Mark where platelets are.
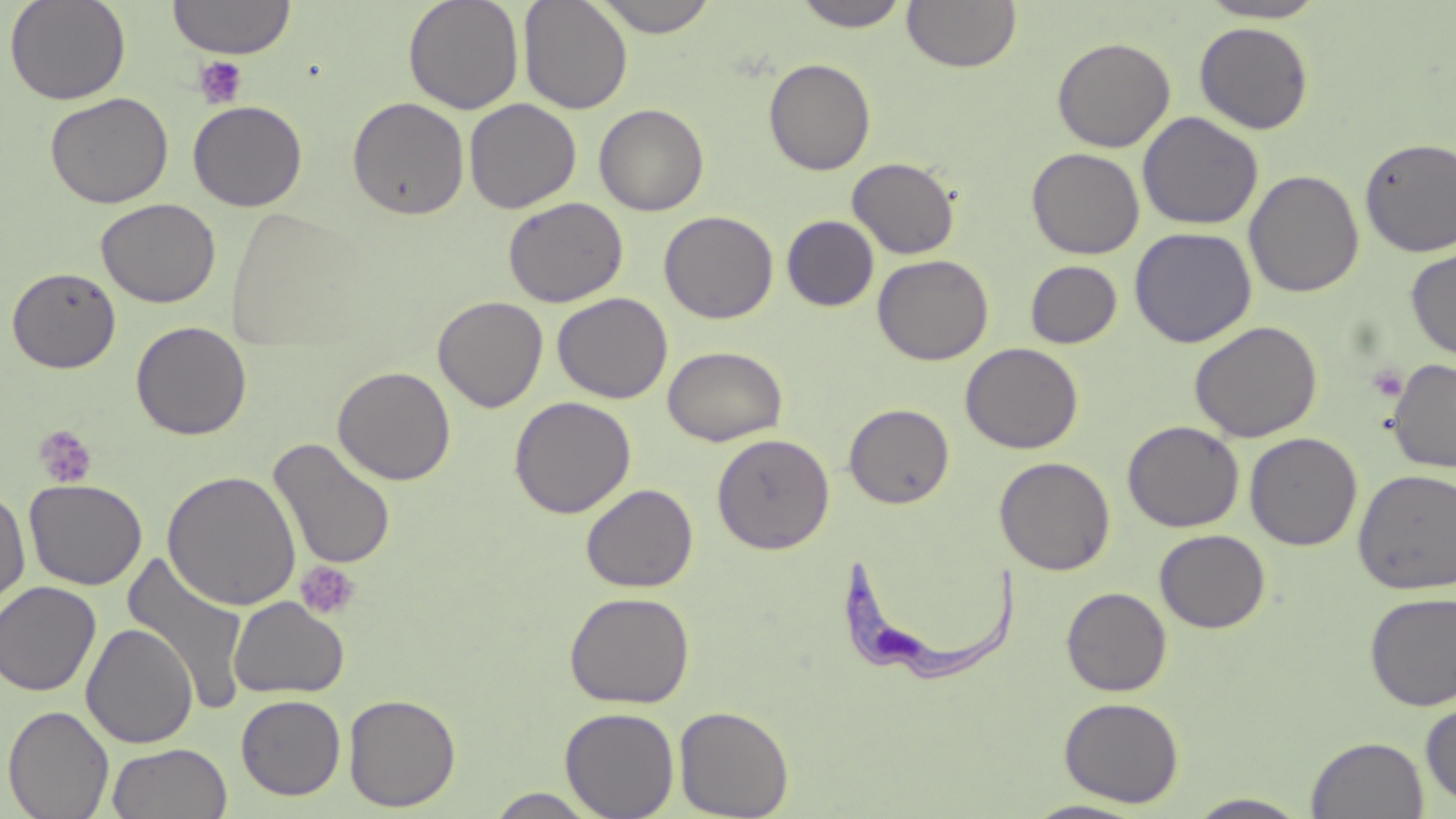

Approximate bounding boxes as (x1, y1, x2, y2) in pixels.
Platelets: (193, 55, 248, 109), (1366, 365, 1409, 402), (34, 425, 97, 489), (295, 561, 361, 621).

Summary:
  - Trypanosoma brucei locations: (844, 553, 1020, 686)
  - Uninfected red blood cell locations: (3, 0, 130, 105), (167, 0, 296, 59), (403, 0, 525, 115), (518, 0, 633, 114), (592, 0, 719, 36), (791, 0, 913, 32), (903, 1, 1021, 73), (1197, 1, 1328, 23), (1194, 21, 1314, 134), (1052, 36, 1175, 152), (764, 58, 876, 175), (45, 92, 174, 209), (347, 96, 470, 220), (464, 98, 582, 214), (188, 100, 307, 211), (594, 103, 709, 216), (1137, 111, 1263, 230), (1358, 136, 1456, 257), (1027, 147, 1145, 259), (848, 157, 960, 259), (1244, 169, 1365, 298), (503, 197, 628, 307), (95, 198, 221, 308), (659, 210, 778, 323), (782, 215, 879, 311), (1130, 227, 1257, 348), (1405, 247, 1456, 362), (873, 254, 994, 365), (1025, 260, 1122, 348), (7, 267, 121, 373), (552, 292, 673, 404), (432, 296, 548, 413), (1189, 320, 1323, 443), (131, 321, 252, 440), (960, 342, 1083, 454), (663, 345, 788, 446), (1387, 358, 1456, 473), (332, 365, 456, 485), (509, 396, 636, 519), (844, 403, 954, 509), (1122, 420, 1244, 532), (711, 432, 835, 554), (1245, 433, 1362, 550), (267, 437, 397, 570), (994, 456, 1116, 575), (1354, 468, 1456, 595), (162, 470, 301, 611), (24, 479, 148, 590), (581, 483, 698, 592), (0, 488, 31, 611), (1154, 529, 1270, 633), (121, 552, 251, 714), (0, 581, 101, 697), (1061, 587, 1171, 696), (564, 590, 695, 708), (1364, 591, 1456, 711), (229, 596, 349, 699), (81, 623, 198, 748), (344, 693, 461, 812), (235, 694, 346, 800), (1059, 697, 1184, 808), (1420, 700, 1456, 811), (2, 705, 115, 819), (674, 705, 794, 818), (560, 706, 680, 819), (1306, 735, 1429, 818), (107, 743, 232, 819), (485, 788, 603, 818), (1185, 793, 1313, 818), (1019, 799, 1151, 818)
  - Slide-level diagnosis: Trypanosoma brucei
  - Image size: 1456×819 pixels
  - Field of view: single
  - Magnification: 1000x
  - Stain: May-Grünwald-Giemsa
  - Preparation: thin blood smear
  - Modality: light microscopy